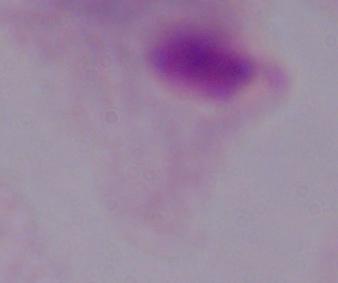
A trichomonad is seen. 1000x magnification. Photomicrograph.